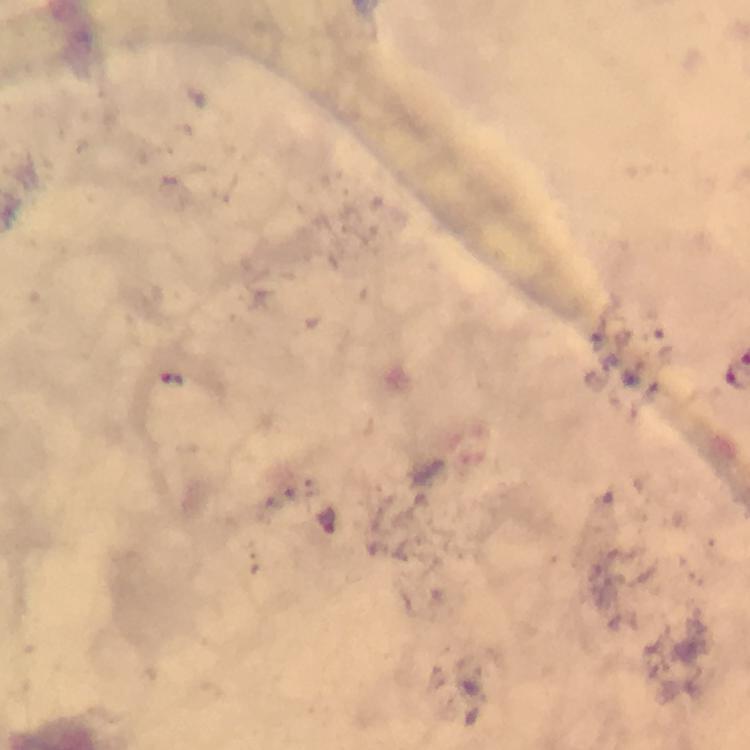
stain: Giemsa
capture: smartphone camera through the microscope
preparation: thick blood smear
immersion_oil: applied
image_size: 750×750 pixels
plasmodium_parasite_locations: 'approximate centers as {x, y} in pixels: {330, 521}'
cropped_from: a single field of view
context: from a malaria diagnostic workup
magnification: 100x